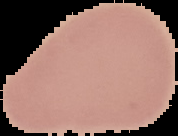
image size = 178×136 pixels
image type = cell region segmented out of the field of view; surrounding area masked to black
preparation = thin blood smear
malaria status = uninfected